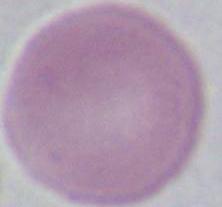

modality = micrograph
magnification = 1000x
identification = erythrocyte